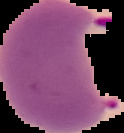
From a thin blood film. Cell region segmented out of the field of view; the surrounding area is masked to black. Image is 124×133 pixels. Result: Plasmodium parasites detected.